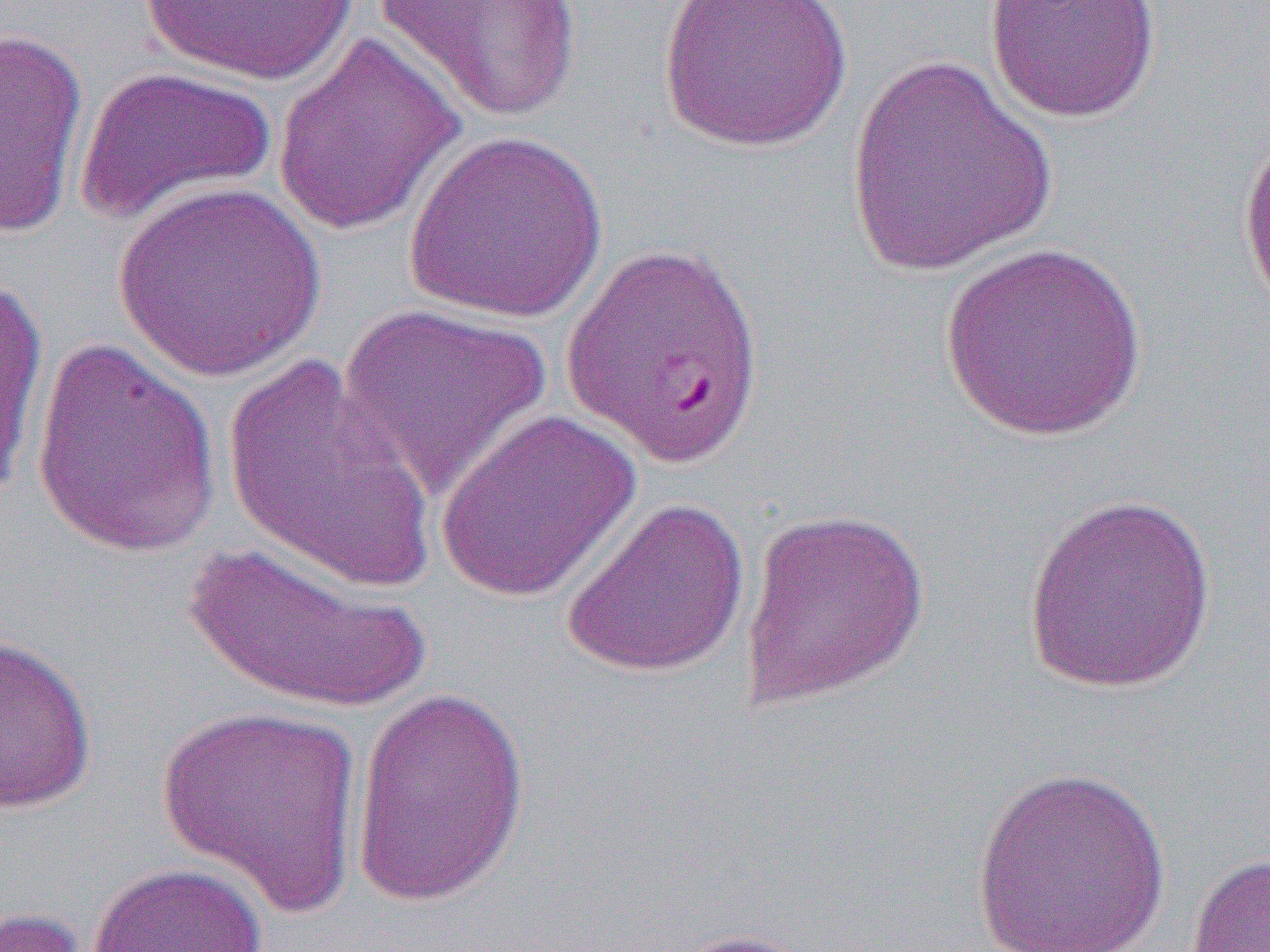
Approximate bounding boxes as (x1, y1, x2, y2) in pixels. Uninfected red blood cell locations: (136, 0, 363, 86), (373, 0, 583, 125), (657, 0, 852, 153), (984, 0, 1161, 124), (0, 25, 90, 242), (271, 32, 466, 240), (842, 53, 1061, 278), (73, 64, 277, 229), (1236, 124, 1270, 317), (404, 129, 609, 325), (111, 181, 328, 382), (937, 242, 1147, 443), (0, 271, 49, 514), (337, 304, 554, 501), (30, 335, 223, 561), (220, 352, 441, 596), (434, 407, 644, 603), (1021, 493, 1218, 695), (560, 494, 751, 680), (739, 507, 931, 711), (180, 541, 432, 718), (0, 634, 98, 814), (348, 684, 532, 910), (157, 703, 365, 916), (969, 764, 1172, 952), (1185, 851, 1270, 952), (87, 861, 269, 952), (0, 906, 92, 952), (657, 927, 834, 952). Slide-level diagnosis: Plasmodium falciparum. Single field of view. Image is 1270×952 pixels. Optical microscopy. Thin blood film. Captured at 1000x magnification.